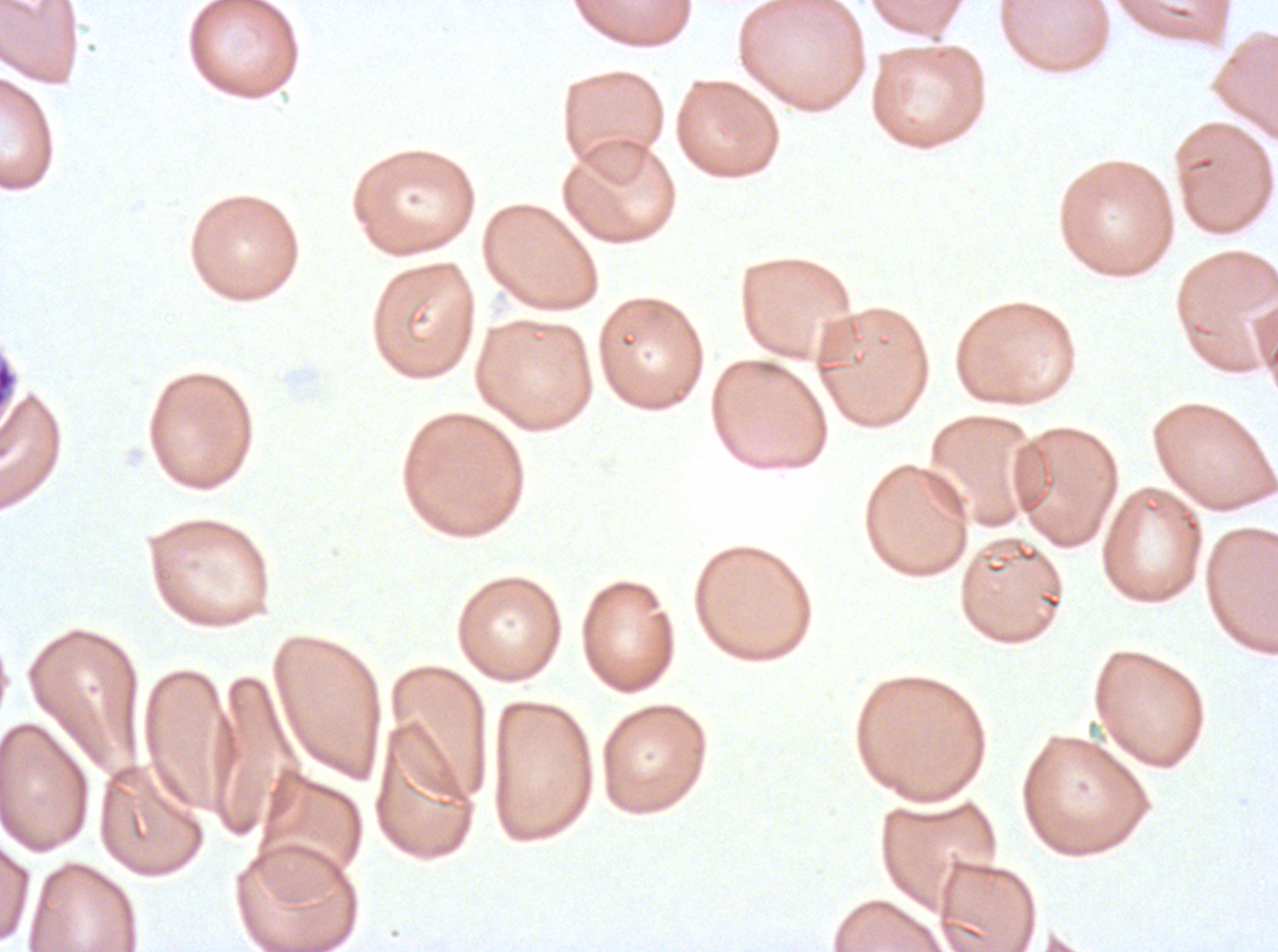
{
  "stain": "Giemsa",
  "specimen": "Plasmodium falciparum from a patient in The Gambia, cultured ex vivo for 24 to 48 hours",
  "late_schizont_locations": "approximate bounding boxes as [x1, y1, x2, y2] in pixels: [0, 360, 17, 408]",
  "image_size": "1278×952 pixels",
  "field_of_view": "sub-image separated from a larger composite",
  "preparation": "thin blood film"
}